State which parasite is depicted.
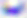

This is Toxoplasma gondii.

Summary:
  - Magnification: 400x
  - Modality: micrograph